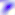
magnification = 400x
identification = Toxoplasma gondii
modality = photomicrograph